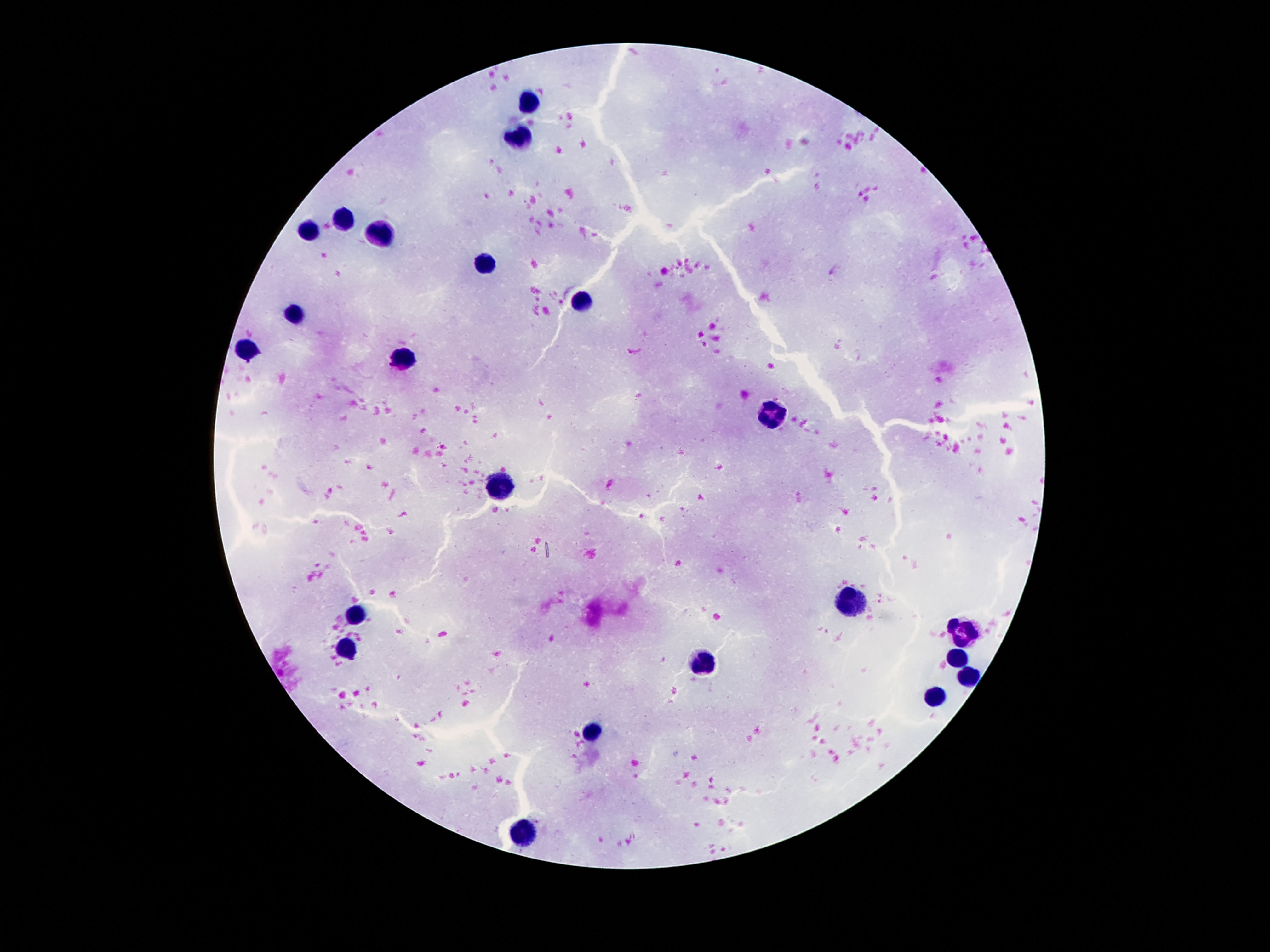

Approximate centers as {x, y} in pixels. Leukocyte locations: {532, 101}, {523, 135}, {341, 220}, {307, 232}, {380, 233}, {486, 265}, {581, 301}, {296, 311}, {244, 352}, {404, 360}, {772, 413}, {500, 485}, {852, 605}, {357, 614}, {961, 628}, {345, 649}, {956, 659}, {706, 662}, {969, 676}, {936, 696}, {591, 732}, {525, 830}. Giemsa-stained preparation. Thick blood smear. Single field of view. Photographed through the microscope eyepiece with a smartphone camera. 100x magnification. Image is 1270×952 pixels. Patient malaria status: uninfected.